Locate every blood parasite and identify its species.
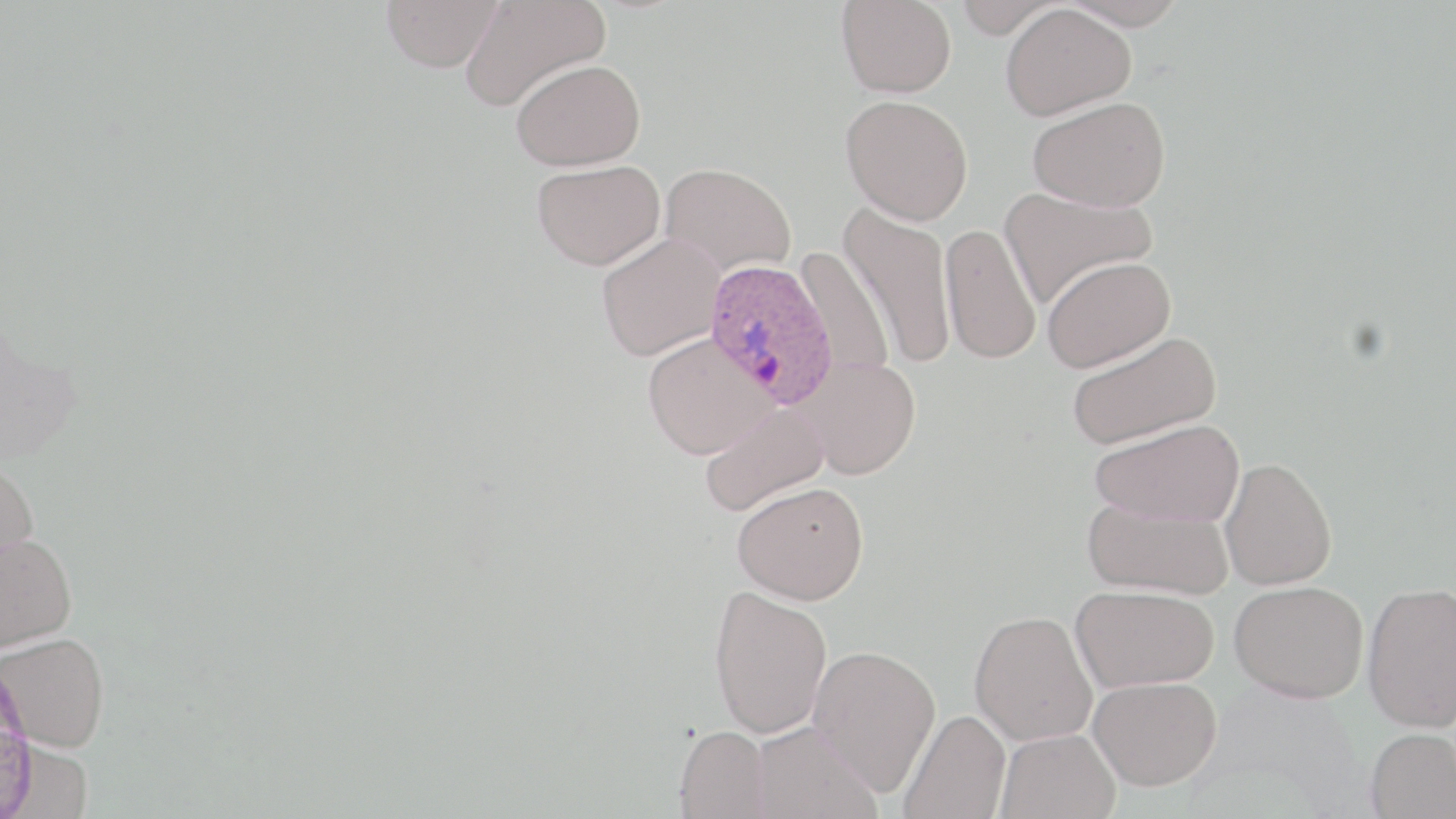
Approximate bounding boxes as named x1/y1/x2/y2 corners in pixels.
Plasmodium ovale-infected red blood cells: (x1=702, y1=257, x2=839, y2=409).
No Plasmodium falciparum, Plasmodium malariae, Plasmodium vivax, Babesia divergens, or Trypanosoma brucei observed.

Summary:
  - Uninfected red blood cell locations: (x1=381, y1=0, x2=503, y2=73), (x1=837, y1=0, x2=957, y2=98), (x1=953, y1=0, x2=1065, y2=38), (x1=1057, y1=0, x2=1191, y2=30), (x1=459, y1=1, x2=609, y2=112), (x1=1000, y1=3, x2=1135, y2=121), (x1=510, y1=59, x2=645, y2=171), (x1=840, y1=95, x2=973, y2=225), (x1=1028, y1=96, x2=1170, y2=212), (x1=531, y1=159, x2=665, y2=270), (x1=660, y1=161, x2=796, y2=277), (x1=999, y1=187, x2=1157, y2=309), (x1=840, y1=201, x2=957, y2=370), (x1=941, y1=223, x2=1041, y2=364), (x1=595, y1=233, x2=726, y2=360), (x1=794, y1=244, x2=895, y2=381), (x1=1041, y1=255, x2=1176, y2=372), (x1=1065, y1=331, x2=1221, y2=450), (x1=642, y1=333, x2=777, y2=459), (x1=796, y1=356, x2=922, y2=480), (x1=698, y1=402, x2=829, y2=516), (x1=1088, y1=418, x2=1244, y2=526), (x1=0, y1=457, x2=39, y2=573), (x1=1219, y1=457, x2=1337, y2=591), (x1=732, y1=480, x2=869, y2=605), (x1=1083, y1=499, x2=1233, y2=599), (x1=0, y1=532, x2=77, y2=652), (x1=1230, y1=579, x2=1369, y2=703), (x1=1362, y1=581, x2=1456, y2=732), (x1=708, y1=584, x2=833, y2=739), (x1=1070, y1=584, x2=1219, y2=692), (x1=969, y1=609, x2=1098, y2=745), (x1=1, y1=632, x2=109, y2=752), (x1=808, y1=644, x2=941, y2=795), (x1=1088, y1=675, x2=1223, y2=791), (x1=899, y1=709, x2=1011, y2=819), (x1=751, y1=720, x2=882, y2=819), (x1=675, y1=725, x2=771, y2=818), (x1=1365, y1=727, x2=1456, y2=819), (x1=996, y1=728, x2=1121, y2=819)
  - Slide-level diagnosis: Plasmodium ovale
  - Image size: 1456×819 pixels
  - Magnification: 1000x
  - Modality: light microscopy
  - Field of view: one of a larger specimen
  - Preparation: thin blood smear
  - Stain: May-Grünwald-Giemsa